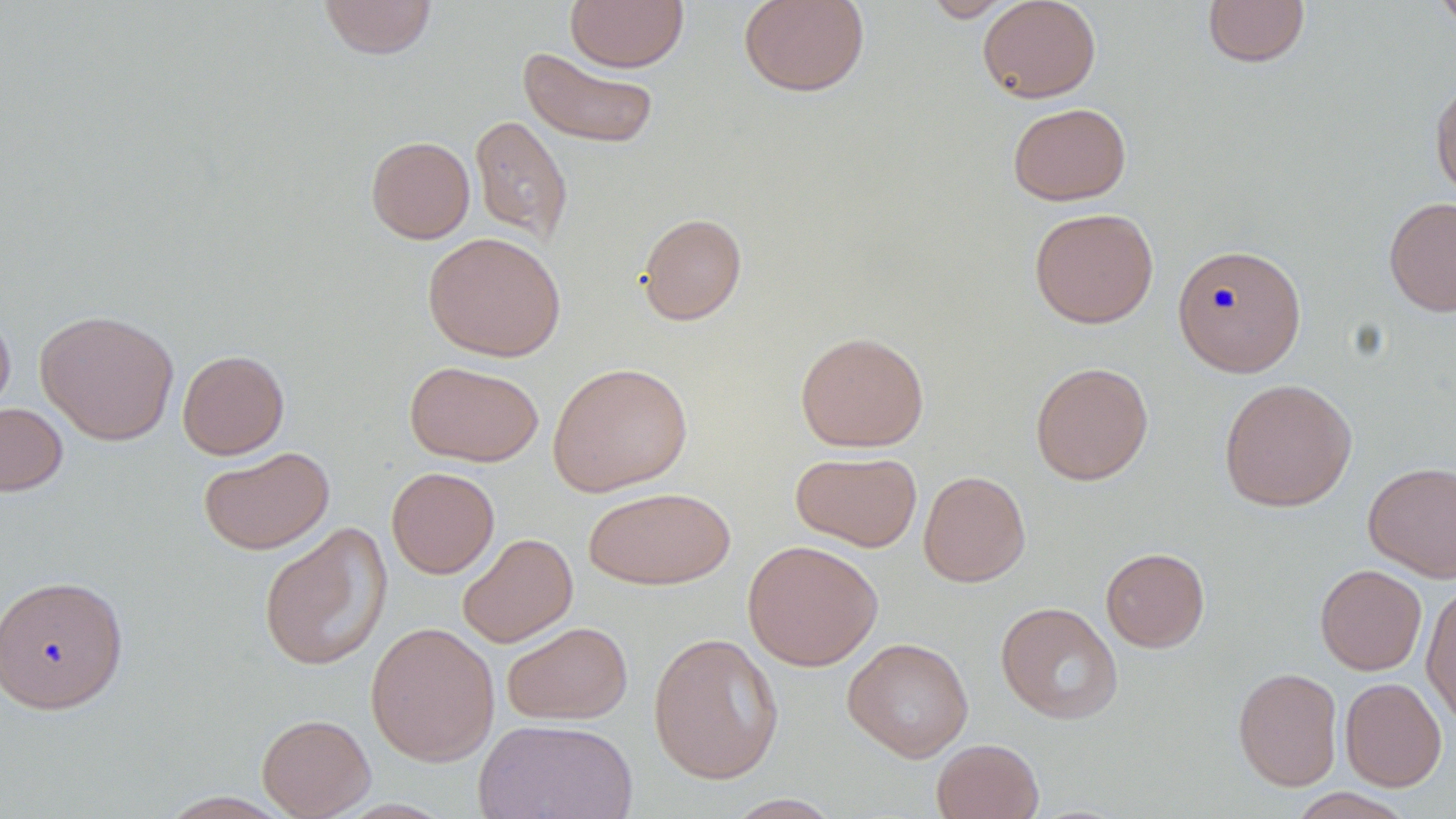

Summary:
  - Coordinate format: approximate bounding boxes as [x1, y1, x2, y2] in pixels
  - Uninfected red blood cell locations: [319, 0, 437, 59], [565, 0, 688, 72], [738, 0, 870, 97], [922, 0, 1019, 22], [978, 0, 1101, 103], [1202, 0, 1310, 68], [1432, 0, 1456, 36], [518, 47, 659, 149], [1431, 78, 1456, 202], [1007, 102, 1131, 205], [470, 114, 573, 244], [366, 136, 475, 243], [1384, 196, 1456, 317], [1029, 207, 1159, 328], [636, 212, 747, 325], [423, 231, 567, 361], [1172, 243, 1307, 377], [0, 304, 15, 418], [35, 309, 179, 446], [795, 331, 929, 452], [177, 349, 289, 459], [405, 360, 543, 466], [547, 361, 693, 497], [1030, 361, 1154, 485], [1218, 377, 1357, 512], [0, 402, 68, 496], [198, 446, 335, 554], [790, 450, 922, 552], [1362, 461, 1456, 583], [386, 466, 499, 579], [917, 470, 1031, 587], [582, 486, 735, 590], [258, 521, 393, 672], [457, 532, 578, 648], [742, 539, 883, 671], [1101, 547, 1210, 652], [1315, 564, 1427, 675], [0, 574, 129, 713], [1421, 582, 1456, 725], [995, 602, 1123, 724], [365, 621, 500, 766], [502, 621, 633, 725], [647, 631, 785, 784], [842, 637, 974, 762], [1233, 666, 1343, 791], [1339, 677, 1447, 791], [257, 713, 375, 819], [475, 718, 638, 819], [931, 738, 1044, 819], [1286, 788, 1416, 819], [157, 791, 295, 818], [721, 793, 844, 818]
  - Slide-level diagnosis: negative for blood parasites
  - Field of view: single
  - Preparation: thin blood film
  - Stain: May-Grünwald-Giemsa
  - Magnification: 1000x
  - Modality: optical microscopy
  - Image size: 1456×819 pixels